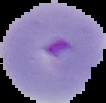

image type = cell region segmented out of the field of view; surrounding area masked to black
preparation = thin blood smear
result = Plasmodium parasites identified
image size = 106×103 pixels